Point out each leukocyte.
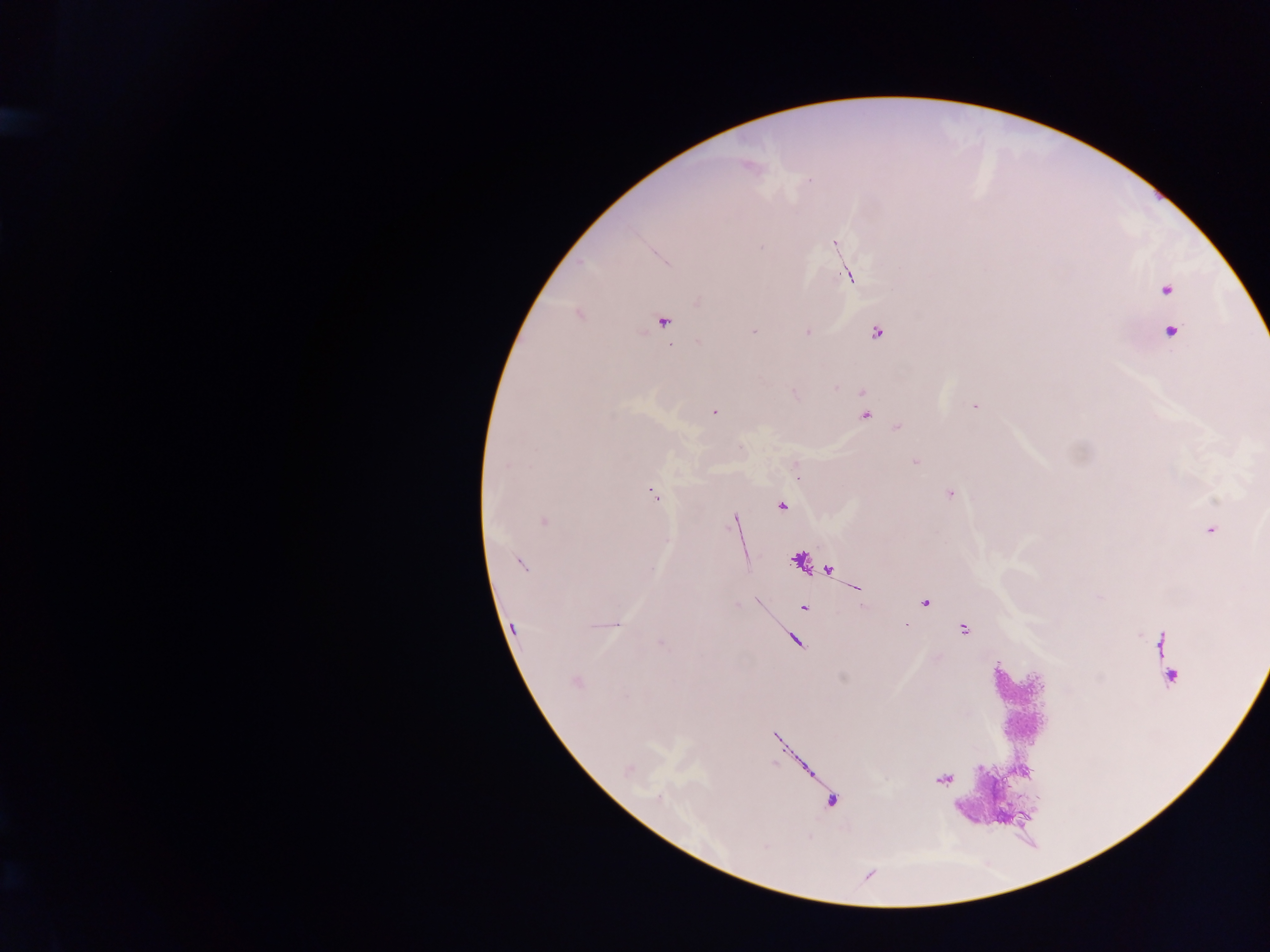
Approximate centers as [x, y] in pixels.
Leukocytes: [1021, 701], [986, 793].

Plasmodium parasite locations: [809, 181], [835, 243], [761, 247], [846, 277], [1166, 290], [579, 315], [664, 322], [1171, 331], [753, 332], [807, 332], [877, 333], [699, 341], [836, 388], [794, 392], [862, 394], [975, 406], [714, 413], [866, 415], [897, 428], [915, 461], [506, 466], [653, 494], [950, 494], [781, 505], [734, 520], [544, 521], [1210, 530], [521, 564], [924, 603], [804, 608], [616, 625], [513, 627], [963, 629], [661, 643], [1170, 677], [576, 682], [944, 779], [658, 797]. Collected in Ghana. Single field of view. Mobile-phone photograph taken through the microscope. Thick blood smear. Image is 1270×952 pixels.